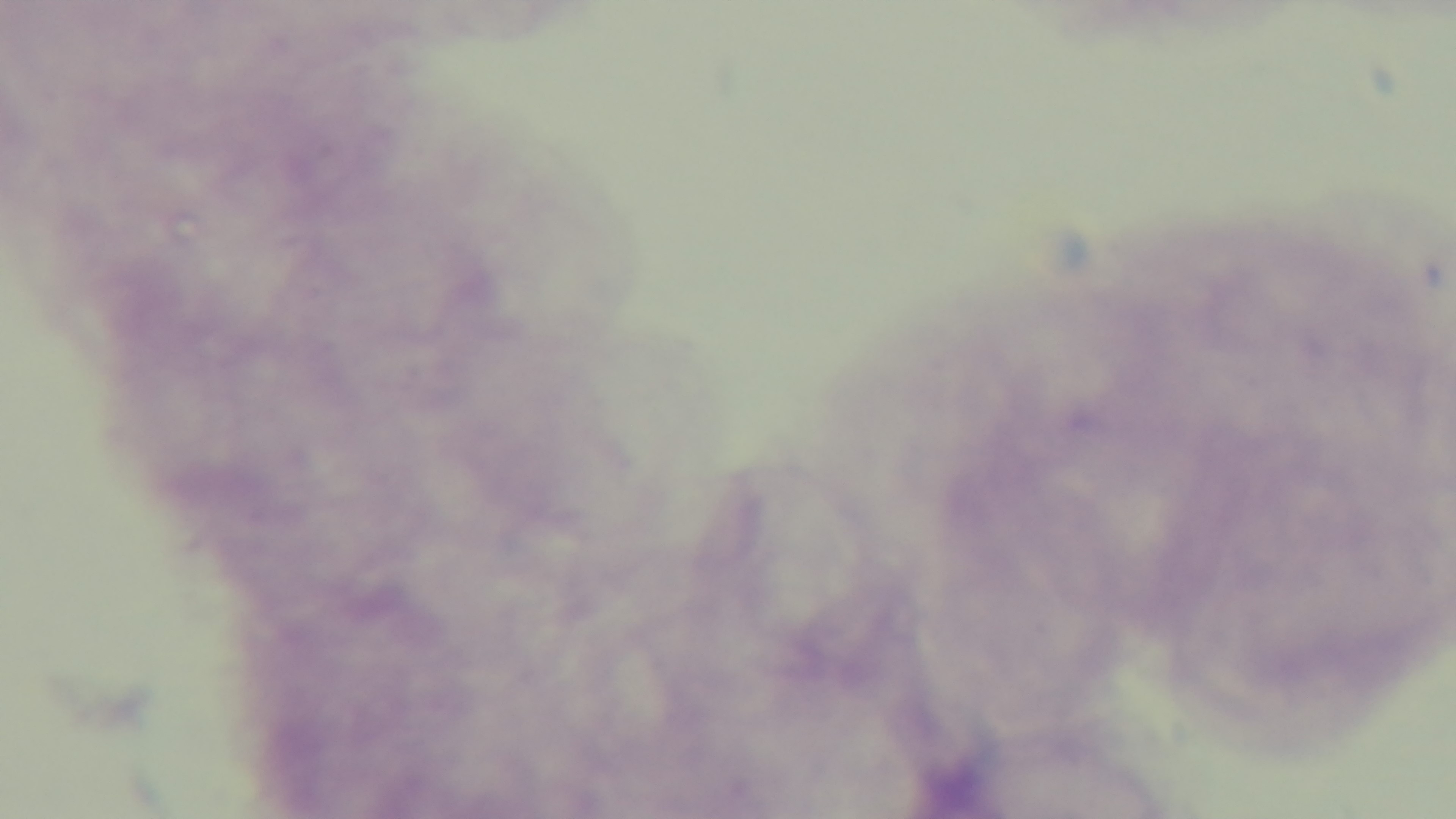

Oil-immersion objective, 100x. Malaria status: negative. Mounted 4K digital camera. Single field of view. Preparation: thick blood film. Giemsa stain. Photomicrograph.